Locate and identify every blood parasite.
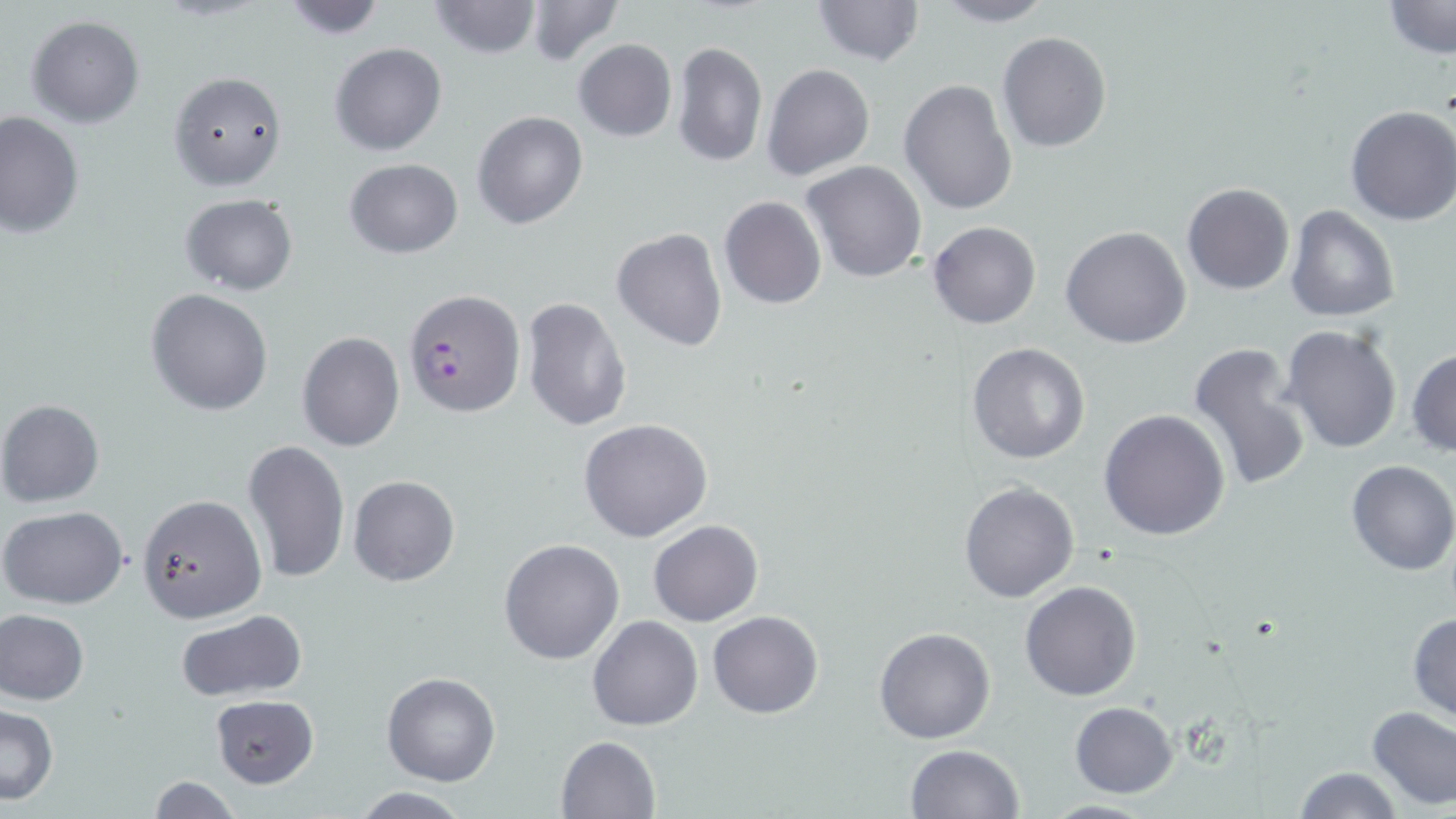
Approximate bounding boxes as named x1/y1/x2/y2 corners in pixels.
Plasmodium falciparum-infected red blood cells: (x1=402, y1=287, x2=525, y2=418).
No Plasmodium ovale, Plasmodium malariae, Plasmodium vivax, Babesia divergens, or Trypanosoma brucei observed.

Summary:
  - Uninfected red blood cell locations: (x1=277, y1=0, x2=389, y2=39), (x1=426, y1=0, x2=544, y2=59), (x1=810, y1=0, x2=925, y2=68), (x1=927, y1=0, x2=1057, y2=28), (x1=1385, y1=0, x2=1456, y2=59), (x1=523, y1=3, x2=625, y2=65), (x1=27, y1=16, x2=144, y2=128), (x1=996, y1=30, x2=1110, y2=154), (x1=572, y1=38, x2=678, y2=142), (x1=330, y1=42, x2=447, y2=157), (x1=672, y1=42, x2=768, y2=168), (x1=762, y1=63, x2=875, y2=181), (x1=166, y1=69, x2=290, y2=191), (x1=898, y1=78, x2=1018, y2=216), (x1=1344, y1=105, x2=1456, y2=226), (x1=471, y1=110, x2=588, y2=230), (x1=0, y1=111, x2=84, y2=240), (x1=344, y1=157, x2=464, y2=258), (x1=801, y1=162, x2=927, y2=282), (x1=1181, y1=183, x2=1294, y2=296), (x1=180, y1=193, x2=298, y2=296), (x1=718, y1=194, x2=827, y2=310), (x1=1285, y1=205, x2=1400, y2=324), (x1=928, y1=221, x2=1040, y2=330), (x1=1061, y1=226, x2=1191, y2=349), (x1=611, y1=227, x2=727, y2=353), (x1=146, y1=289, x2=273, y2=415), (x1=521, y1=296, x2=632, y2=433), (x1=1280, y1=324, x2=1402, y2=453), (x1=296, y1=330, x2=405, y2=453), (x1=1188, y1=341, x2=1313, y2=489), (x1=967, y1=343, x2=1089, y2=464), (x1=1407, y1=346, x2=1456, y2=456), (x1=0, y1=399, x2=105, y2=507), (x1=1098, y1=409, x2=1230, y2=541), (x1=579, y1=418, x2=713, y2=542), (x1=243, y1=438, x2=350, y2=585), (x1=1345, y1=460, x2=1456, y2=575), (x1=349, y1=475, x2=459, y2=587), (x1=959, y1=480, x2=1079, y2=603), (x1=138, y1=493, x2=267, y2=623), (x1=1, y1=507, x2=128, y2=608), (x1=648, y1=519, x2=763, y2=625), (x1=498, y1=537, x2=624, y2=665), (x1=1020, y1=581, x2=1142, y2=701), (x1=1, y1=610, x2=88, y2=704), (x1=174, y1=610, x2=306, y2=702), (x1=706, y1=610, x2=822, y2=718), (x1=1407, y1=612, x2=1456, y2=724), (x1=587, y1=615, x2=703, y2=731), (x1=874, y1=627, x2=997, y2=744), (x1=382, y1=673, x2=500, y2=786), (x1=211, y1=693, x2=320, y2=788), (x1=1069, y1=702, x2=1178, y2=798), (x1=0, y1=704, x2=60, y2=805), (x1=1365, y1=707, x2=1456, y2=811), (x1=555, y1=735, x2=660, y2=819), (x1=904, y1=744, x2=1023, y2=819), (x1=1292, y1=765, x2=1406, y2=819), (x1=145, y1=775, x2=242, y2=818), (x1=347, y1=788, x2=474, y2=817), (x1=1038, y1=799, x2=1162, y2=818)
  - Slide-level diagnosis: Plasmodium falciparum
  - Image size: 1456×819 pixels
  - Magnification: 1000x
  - Preparation: thin blood smear
  - Modality: optical microscopy
  - Stain: May-Grünwald-Giemsa
  - Field of view: single